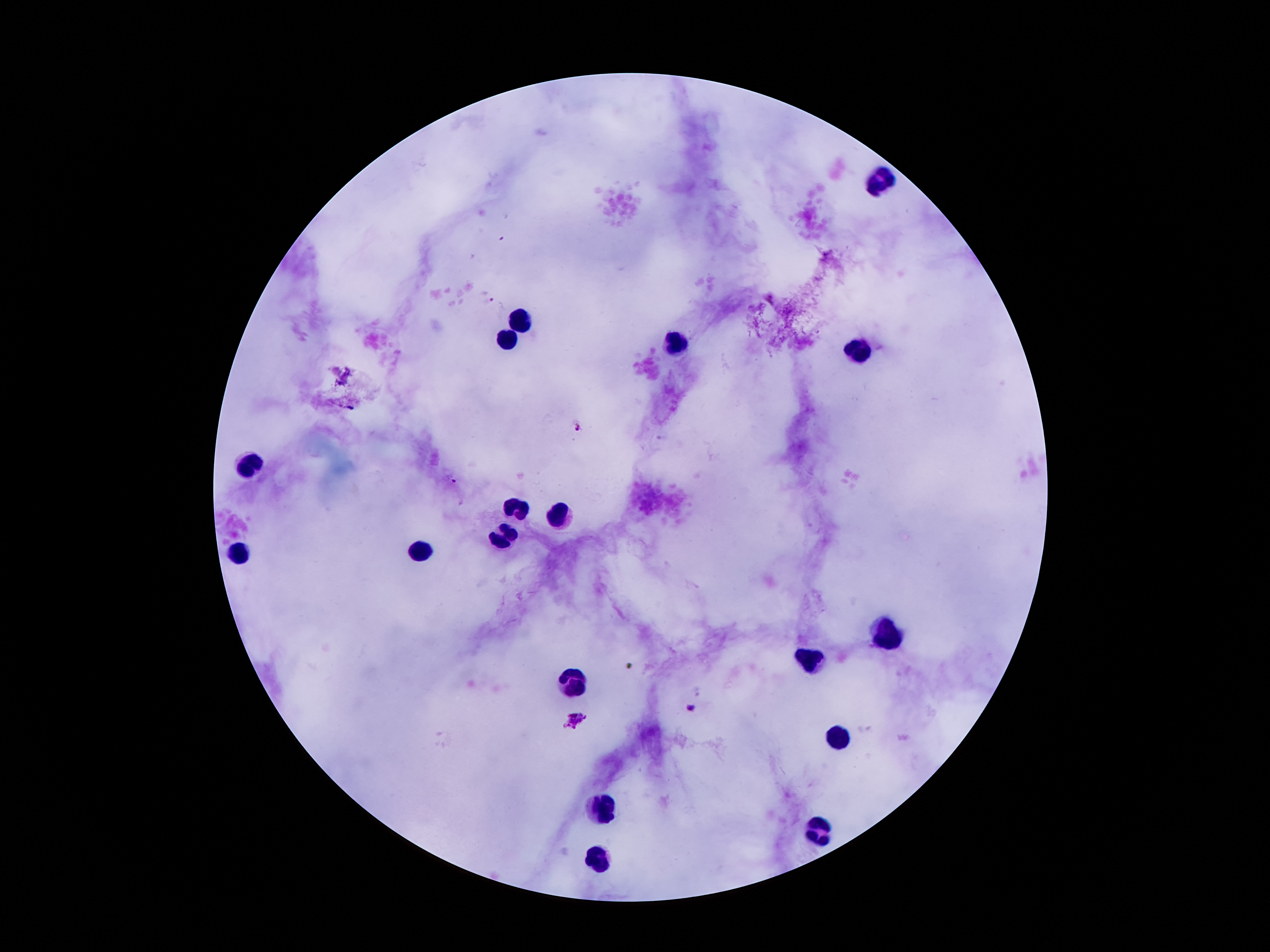

coordinate format = approximate centers as (x, y) in pixels
malaria parasite locations = (504, 238), (492, 299), (578, 426), (453, 481), (690, 708), (578, 719)
leukocyte locations = (884, 181), (521, 318), (504, 339), (678, 345), (857, 353), (250, 469), (519, 507), (559, 507), (504, 536), (242, 551), (424, 551), (890, 637), (806, 664), (575, 681), (836, 742), (601, 809), (819, 832), (599, 859)
stain = Giemsa
image size = 1270×952 pixels
preparation = thick blood smear
capture = smartphone through the microscope eyepiece
magnification = 100x
field of view = single
patient malaria status = infected with Plasmodium falciparum